Identify the blood parasite species.
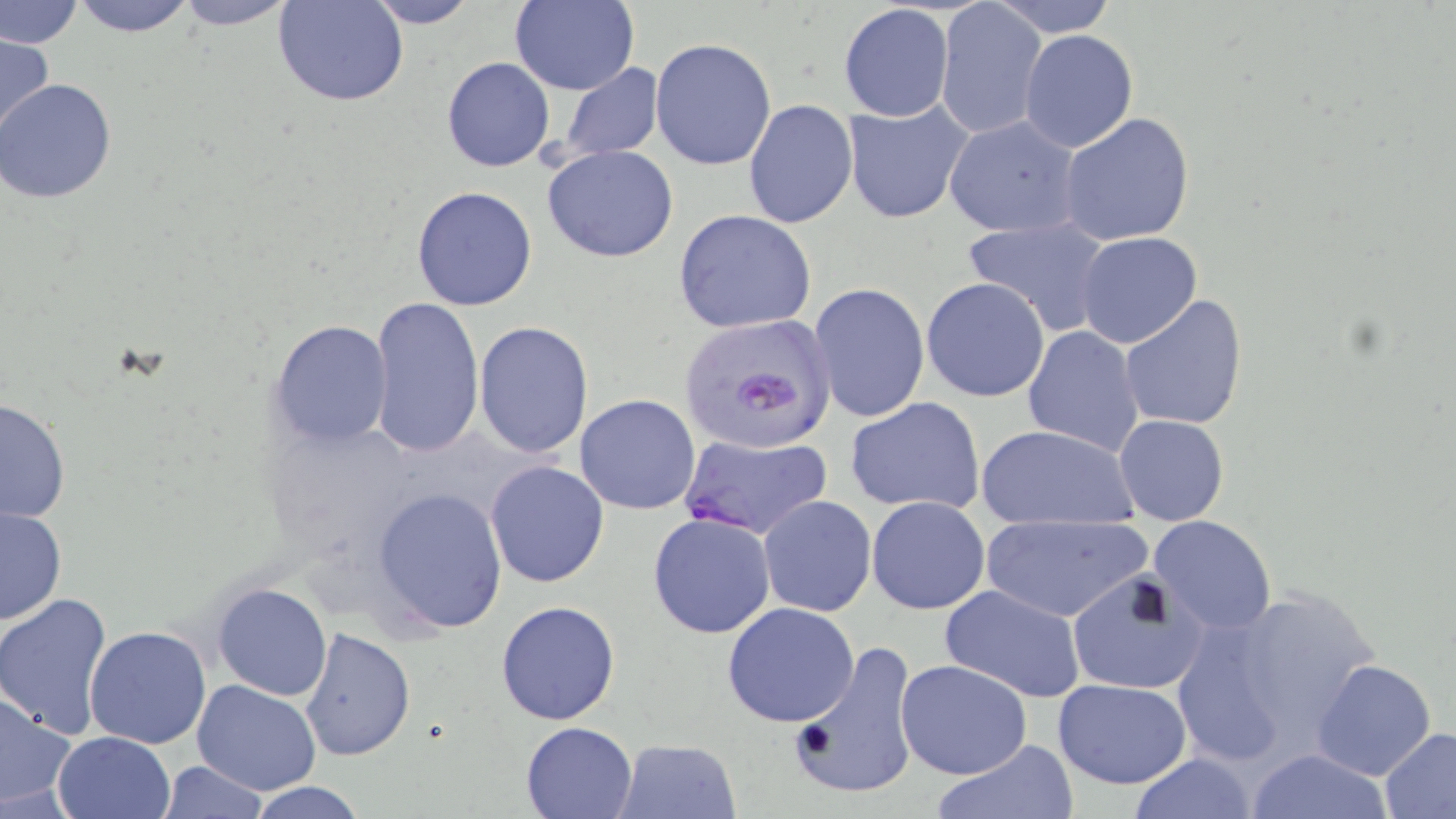

Plasmodium falciparum.

Summary:
  - Coordinate format: approximate bounding boxes as [x1, y1, x2, y2] in pixels
  - Plasmodium falciparum-infected red blood cell locations: [677, 314, 838, 458], [677, 431, 833, 542]
  - Uninfected red blood cell locations: [0, 0, 84, 50], [66, 0, 202, 36], [171, 0, 302, 29], [508, 0, 639, 96], [275, 1, 407, 107], [361, 1, 479, 28], [935, 1, 1046, 140], [989, 1, 1119, 38], [837, 3, 954, 123], [1018, 29, 1140, 153], [0, 32, 56, 143], [649, 38, 777, 170], [440, 56, 555, 173], [558, 63, 664, 162], [0, 79, 117, 203], [742, 97, 857, 230], [842, 100, 974, 225], [1059, 113, 1196, 248], [943, 115, 1081, 238], [542, 145, 679, 263], [411, 186, 540, 312], [674, 209, 817, 335], [960, 215, 1112, 336], [1074, 231, 1204, 349], [921, 276, 1050, 403], [809, 283, 930, 423], [1120, 293, 1249, 431], [369, 295, 484, 457], [268, 319, 393, 449], [474, 322, 595, 458], [1022, 325, 1145, 456], [574, 394, 701, 514], [1, 396, 72, 526], [844, 396, 988, 515], [1114, 414, 1229, 525], [975, 423, 1141, 531], [484, 459, 611, 588], [372, 487, 508, 632], [758, 495, 876, 616], [866, 495, 990, 614], [1, 506, 68, 627], [647, 511, 776, 639], [977, 512, 1153, 623], [1148, 516, 1277, 637], [1063, 574, 1213, 700], [211, 583, 333, 701], [939, 584, 1087, 704], [1174, 590, 1382, 764], [0, 592, 115, 739], [495, 600, 622, 725], [721, 601, 860, 727], [84, 625, 213, 749], [299, 627, 416, 762], [788, 639, 921, 803], [896, 658, 1033, 780], [1312, 659, 1438, 782], [1052, 678, 1192, 787], [192, 679, 321, 795], [0, 690, 78, 814], [520, 721, 637, 818], [1378, 727, 1456, 817], [52, 731, 176, 819], [615, 736, 742, 818], [931, 739, 1079, 819], [1248, 747, 1393, 819], [1128, 752, 1258, 819], [156, 761, 268, 818], [244, 780, 370, 818]
  - Image size: 1456×819 pixels
  - Stain: May-Grünwald-Giemsa
  - Field of view: single
  - Preparation: thin blood smear
  - Magnification: 1000x
  - Modality: light microscopy